Assess this cell for malaria.
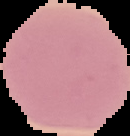

Uninfected.

From a thin blood smear. Image is 130×136 pixels. Segmented cell region on a black background.